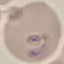
result = malaria parasites detected
stain = Giemsa
capture = smartphone through the microscope eyepiece
preparation = thin blood smear
image type = automatically extracted cell patch, resized to 64 × 64 pixels